Assess this cell for malaria.
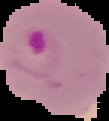

It is parasitized.

Cell region segmented out of the field of view; the surrounding area is masked to black. Image is 109×121 pixels. From a thin blood film.